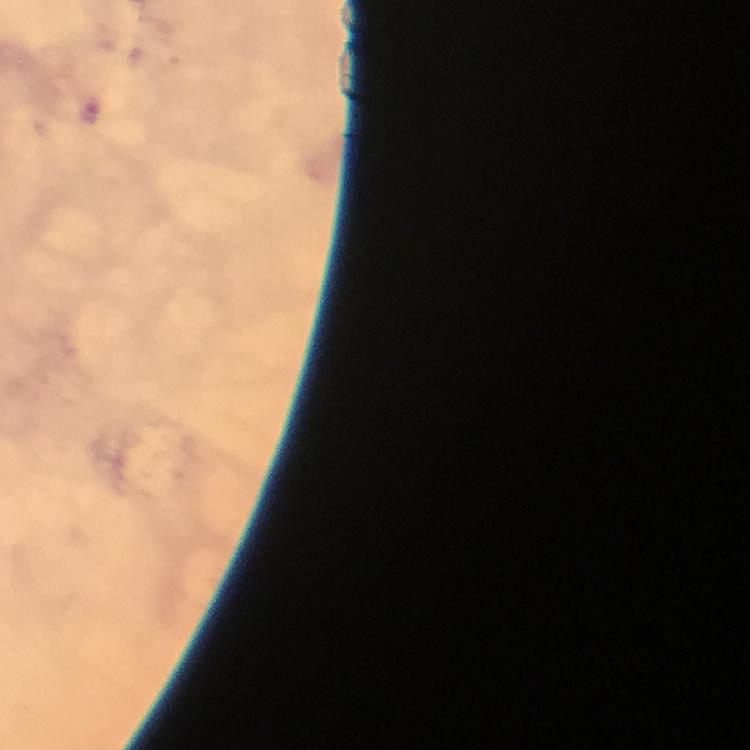

Approximate centers as [x, y] in pixels.
Summary:
  - Malaria parasite locations: [92, 109]
  - Capture: smartphone photograph through a microscope
  - Preparation: thick smear
  - Context: from a malaria diagnostic workup
  - Cropped from: a single field of view
  - Image size: 750×750 pixels
  - Stain: Giemsa
  - Immersion oil: applied
  - Magnification: 100x